Classify this cell by malaria status.
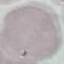
It is uninfected.

Summary:
  - Capture: smartphone through the microscope eyepiece
  - Preparation: thin smear
  - Image type: automatically extracted cell patch, resized to 64 × 64 pixels
  - Stain: Giemsa